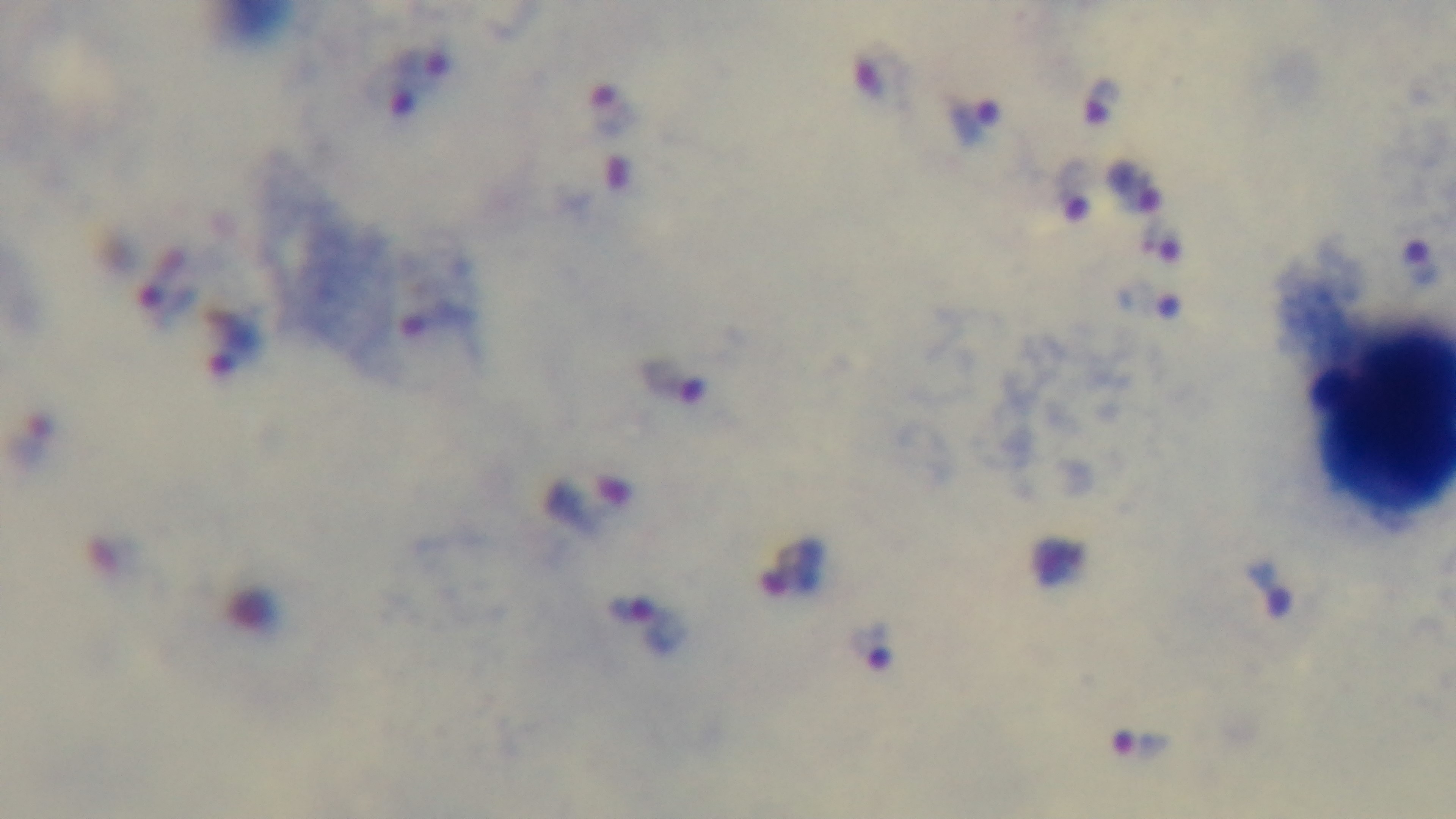

preparation: thick blood film
field_of_view: single
stain: Giemsa
objective: 100x oil immersion
modality: light microscopy
malaria_status: infected
capture: mounted 4K digital camera